Assess the morphology of the erythrocytes.
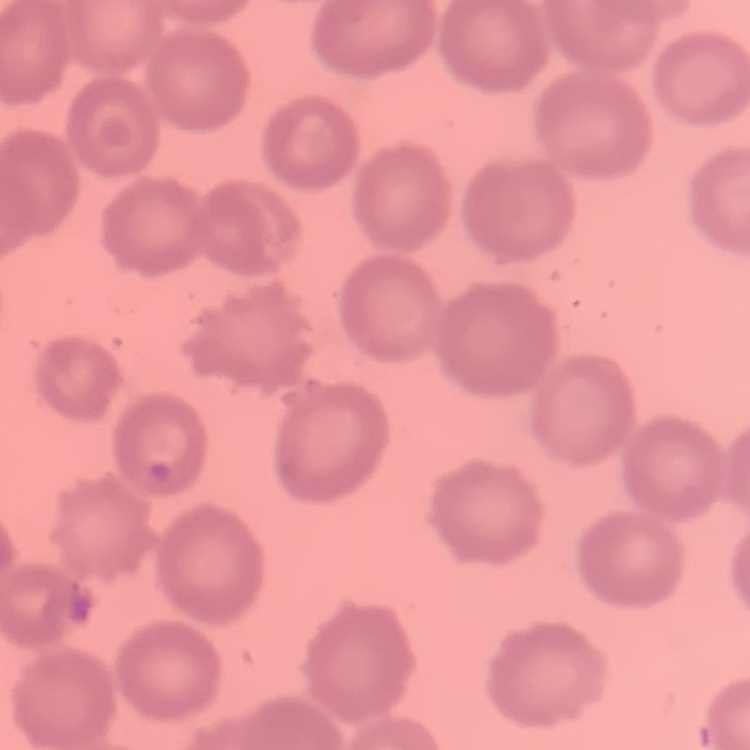

No rouleaux formation.

stain = Field's or Giemsa
image type = square crop of a larger photomicrograph
preparation = thin peripheral smear